Outline each Plasmodium falciparum-infected red blood cell.
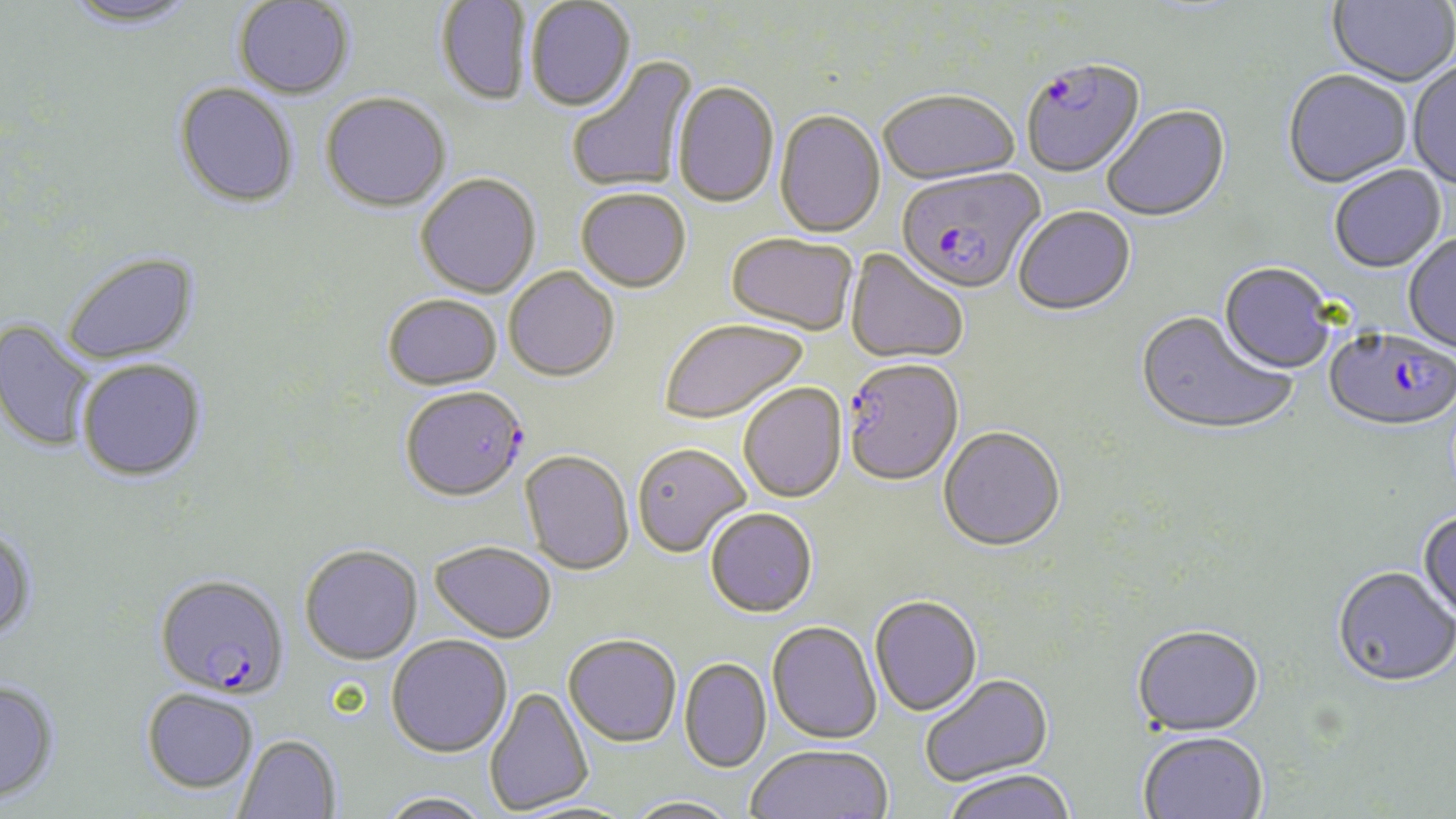

Approximate bounding boxes as (x1,y1)-(x2,y2) corner pairs in pixels.
Plasmodium falciparum-infected red blood cells: (1022,61)-(1148,182), (895,170)-(1045,297), (1324,330)-(1455,435), (841,361)-(964,489), (400,386)-(528,502), (153,572)-(290,698).

slide-level diagnosis = Plasmodium falciparum
modality = optical microscopy
preparation = thin blood smear
magnification = 1000x
image size = 1456×819 pixels
stain = May-Grünwald-Giemsa
uninfected red blood cell locations = approximate bounding boxes as (x1,y1)-(x2,y2) corner pairs in pixels: (60,0)-(202,29), (232,0)-(355,99), (1327,0)-(1455,90), (436,1)-(532,107), (525,1)-(636,114), (566,55)-(699,194), (1408,62)-(1456,192), (1282,72)-(1412,191), (173,82)-(300,209), (673,82)-(779,210), (320,93)-(451,213), (878,93)-(1020,187), (1102,107)-(1231,224), (774,112)-(886,239), (1330,166)-(1446,274), (415,174)-(541,299), (576,191)-(691,294), (1013,208)-(1136,318), (726,235)-(858,338), (1403,235)-(1456,355), (844,249)-(968,367), (61,251)-(199,365), (1218,264)-(1335,376), (504,269)-(620,384), (382,294)-(503,391), (1134,312)-(1297,439), (0,320)-(97,453), (660,320)-(808,426), (77,358)-(207,481), (738,384)-(847,505), (938,428)-(1066,554), (631,444)-(751,558), (520,452)-(634,575), (705,508)-(818,617), (1417,512)-(1456,626), (0,525)-(37,642), (430,540)-(556,642), (299,544)-(423,664), (1331,568)-(1456,691), (870,597)-(982,718), (767,621)-(881,745), (1131,628)-(1265,739), (563,633)-(681,747), (385,634)-(512,757), (679,657)-(772,772), (920,674)-(1054,788), (0,679)-(59,804), (483,685)-(594,815), (142,688)-(259,793), (234,734)-(341,819), (1138,734)-(1268,819), (746,744)-(893,819), (941,771)-(1078,819), (379,790)-(492,819), (623,796)-(743,819), (511,800)-(637,819)
field of view = single